State which parasite is depicted.
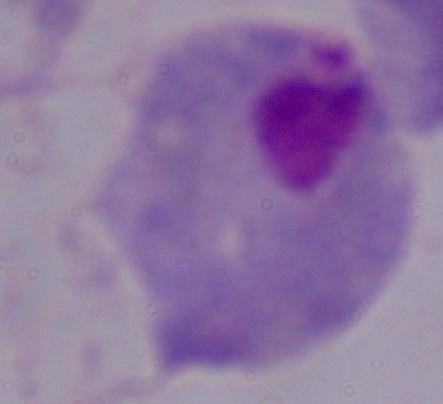

A trichomonad.

1000x magnification. Photomicrograph.